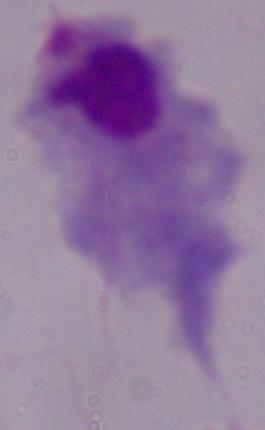
Summary:
  - Identification: trichomonad
  - Modality: photomicrograph
  - Magnification: 1000x